Locate and identify every blood parasite.
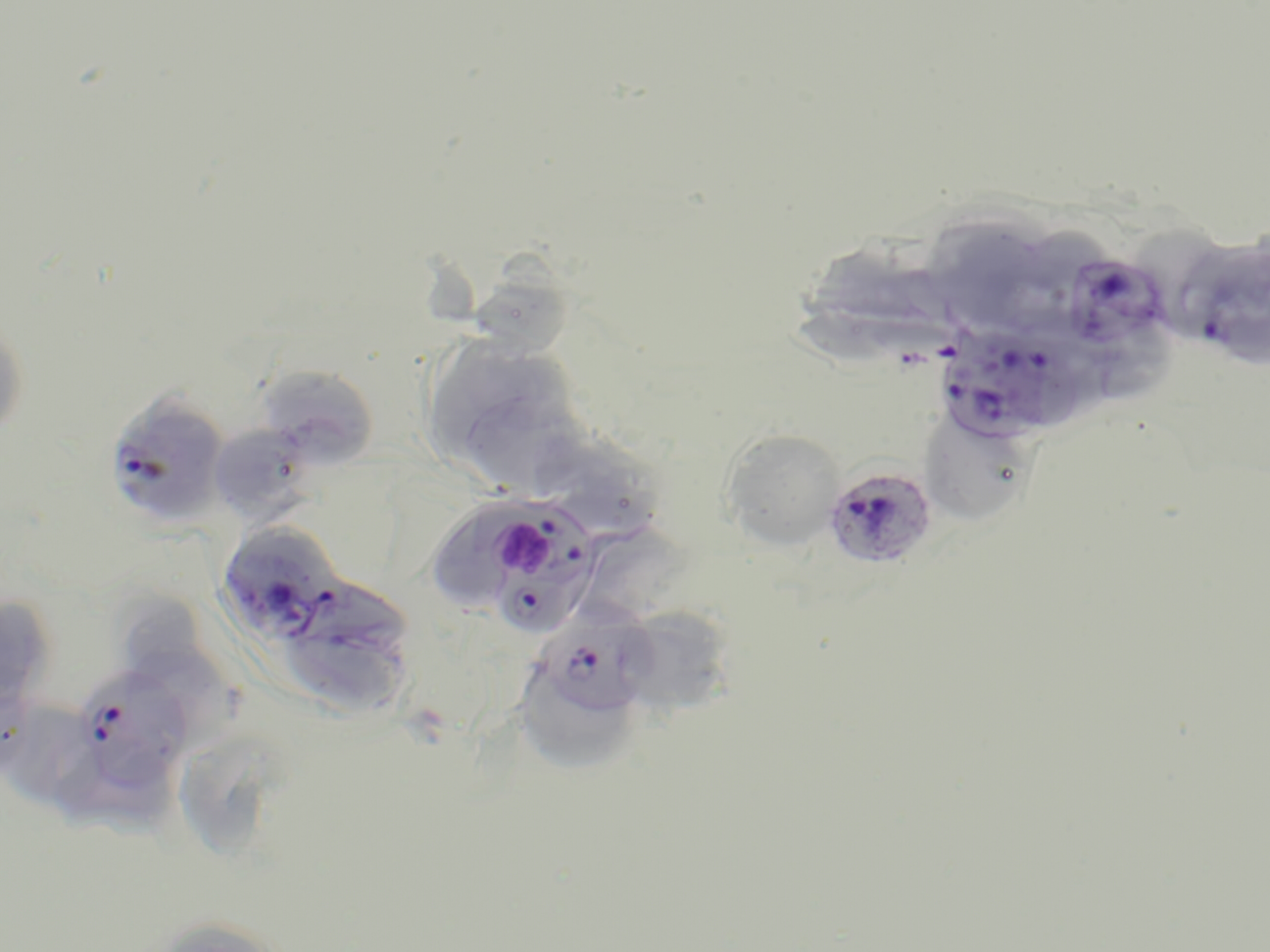

Approximate bounding boxes as named x1/y1/x2/y2 corners in pixels.
Plasmodium falciparum-infected red blood cells: (x1=1069, y1=254, x2=1174, y2=348), (x1=1199, y1=260, x2=1270, y2=368), (x1=934, y1=328, x2=1079, y2=443), (x1=104, y1=391, x2=231, y2=529), (x1=822, y1=466, x2=938, y2=570), (x1=468, y1=495, x2=603, y2=638), (x1=217, y1=520, x2=343, y2=644), (x1=533, y1=615, x2=657, y2=722), (x1=70, y1=664, x2=193, y2=794).
No Plasmodium ovale, Plasmodium malariae, Plasmodium vivax, Babesia divergens, or Trypanosoma brucei observed.

slide-level diagnosis = Plasmodium falciparum
field of view = single
magnification = 1000x
stain = May-Grünwald-Giemsa
uninfected red blood cell locations = approximate bounding boxes as named x1/y1/x2/y2 corners in pixels: (x1=931, y1=214, x2=1042, y2=322), (x1=1133, y1=219, x2=1231, y2=336), (x1=799, y1=245, x2=915, y2=358), (x1=477, y1=248, x2=568, y2=354), (x1=0, y1=316, x2=29, y2=441), (x1=1074, y1=334, x2=1182, y2=408), (x1=420, y1=336, x2=585, y2=487), (x1=255, y1=364, x2=379, y2=467), (x1=919, y1=410, x2=1037, y2=525), (x1=208, y1=423, x2=317, y2=525), (x1=528, y1=423, x2=663, y2=540), (x1=721, y1=428, x2=845, y2=549), (x1=275, y1=580, x2=419, y2=718), (x1=0, y1=595, x2=54, y2=711), (x1=119, y1=598, x2=247, y2=738), (x1=612, y1=605, x2=734, y2=714), (x1=517, y1=673, x2=633, y2=768), (x1=0, y1=697, x2=103, y2=811), (x1=175, y1=753, x2=282, y2=864), (x1=142, y1=916, x2=292, y2=952)
preparation = thin blood smear
platelet locations = approximate bounding boxes as named x1/y1/x2/y2 corners in pixels: (x1=500, y1=520, x2=554, y2=577)
modality = optical microscopy
image size = 1270×952 pixels